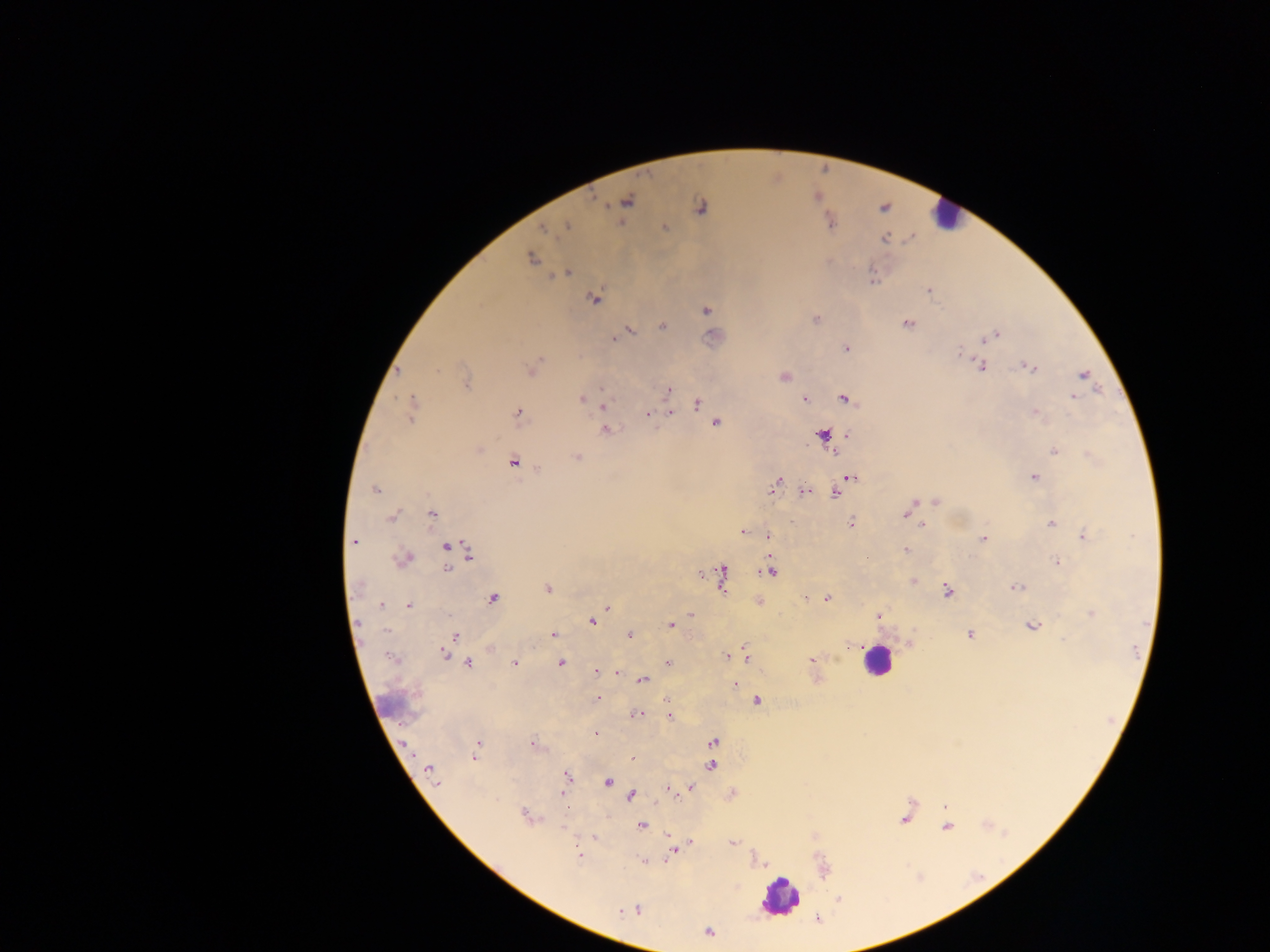

Approximate centers as [x, y] in pixels.
Summary:
  - Leukocyte locations: [946, 214], [878, 661], [780, 896]
  - Plasmodium parasite locations: [626, 201], [699, 207], [829, 221], [567, 226], [664, 227], [543, 229], [884, 238], [531, 257], [568, 272], [929, 290], [594, 298], [706, 310], [815, 319], [908, 323], [661, 326], [629, 329], [995, 335], [613, 338], [846, 349], [959, 351], [979, 365], [1031, 367], [532, 368], [783, 375], [1083, 375], [466, 382], [668, 390], [1074, 396], [582, 399], [805, 399], [844, 399], [587, 401], [668, 401], [697, 404], [602, 405], [412, 408], [1035, 411], [670, 412], [647, 413], [518, 414], [715, 422], [605, 430], [847, 434], [821, 435], [478, 448], [1054, 450], [835, 454], [575, 457], [513, 462], [850, 477], [1034, 477], [775, 484], [375, 489], [804, 491], [836, 492], [936, 500], [909, 508], [431, 514], [392, 515], [850, 523], [1050, 524], [922, 525], [743, 532], [1084, 535], [767, 536], [983, 538], [354, 542], [447, 546], [905, 550], [468, 555], [403, 559], [1057, 562], [447, 568], [770, 571], [721, 576], [913, 581], [1015, 586], [548, 589], [947, 590], [492, 597], [805, 597], [826, 597], [757, 601], [380, 604], [408, 605], [607, 607], [691, 614], [1091, 614], [877, 615], [591, 621], [670, 624], [1031, 626], [553, 634], [629, 634], [970, 634], [456, 636], [910, 642], [852, 644], [491, 648], [444, 652], [726, 656], [745, 656], [392, 658], [812, 660], [467, 662], [513, 662], [560, 663], [667, 663], [617, 671], [596, 672], [641, 680], [735, 684], [597, 697], [668, 699], [757, 700], [635, 714], [670, 717], [595, 733], [712, 741], [477, 745], [533, 745], [475, 753], [632, 757], [711, 765], [430, 771], [566, 777], [607, 781], [689, 788], [667, 789], [563, 791], [732, 793], [631, 795], [945, 807], [526, 815], [904, 818], [641, 825], [946, 826], [593, 837], [689, 842], [733, 843], [673, 850], [580, 856], [645, 861], [636, 909], [628, 910], [817, 918], [708, 931]
  - Preparation: thick blood smear
  - Capture: mobile-phone photograph through a microscope
  - Field of view: single
  - Image size: 1270×952 pixels
  - Country: Ghana